Comment on the morphology of the red blood cells.
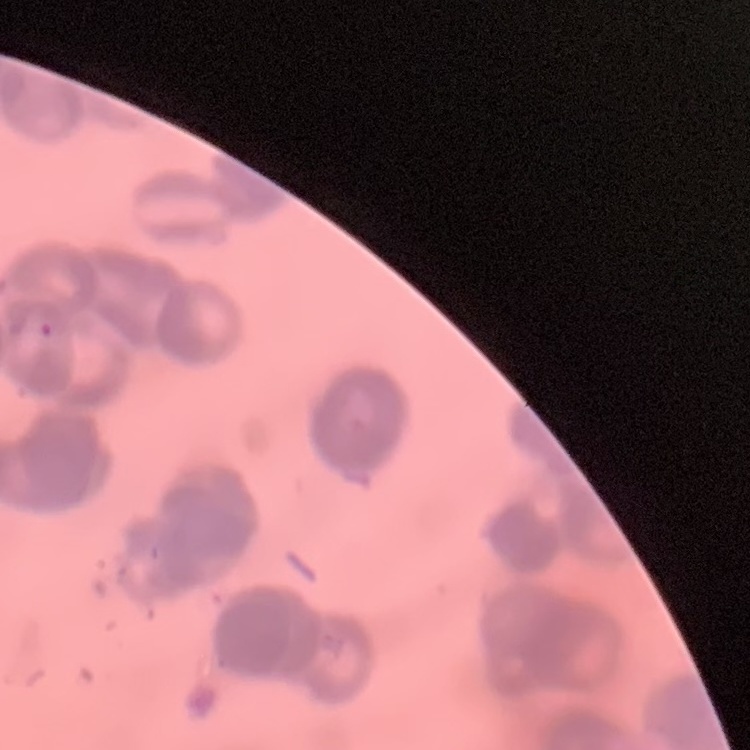

Rouleaux formation.

One tile cut from a larger photomicrograph. Thin blood film. Field's or Giemsa stain.